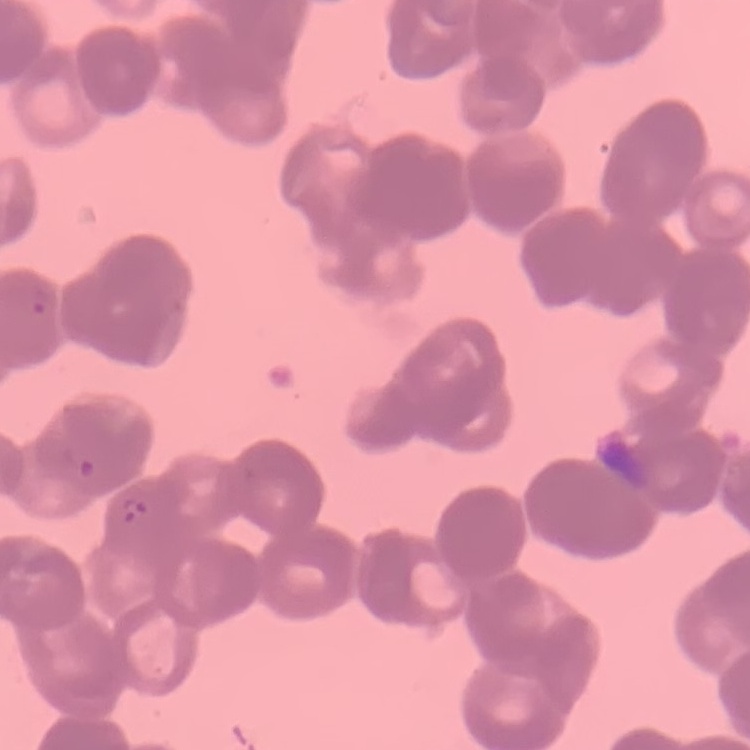 The erythrocytes show rouleaux formation. One tile cut from a larger photomicrograph. Stained with either Field's or Giemsa. Thin blood film.